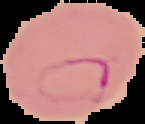

image_size: 145×124 pixels
image_type: segmented cell region with the area outside set to black
preparation: thin blood film
malaria_status: parasitized